Name the parasite shown.
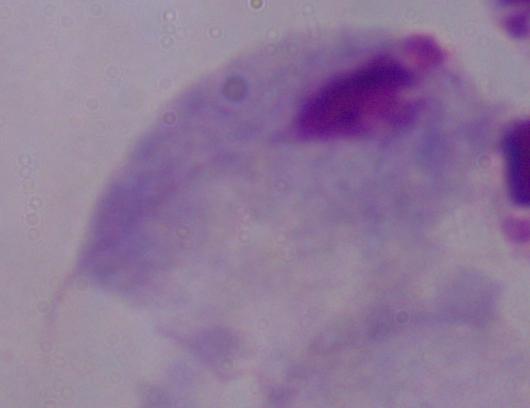

This is a trichomonad.

{
  "modality": "photomicrograph",
  "magnification": "1000x"
}